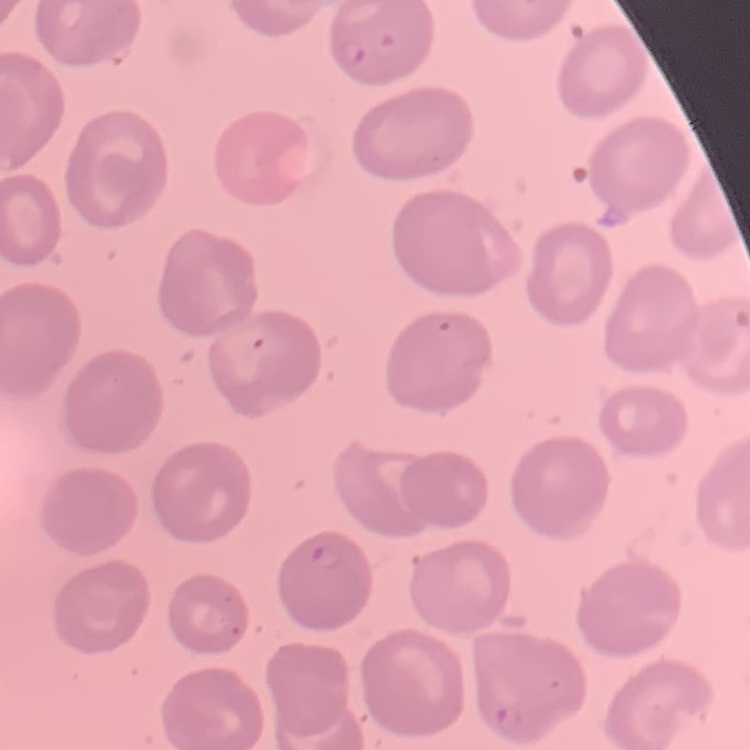
Summary:
  - Erythrocyte morphology: no rouleaux formation
  - Stain: Field's or Giemsa
  - Image type: one tile cut from a larger photomicrograph
  - Preparation: thin blood smear